Locate and identify every blood parasite.
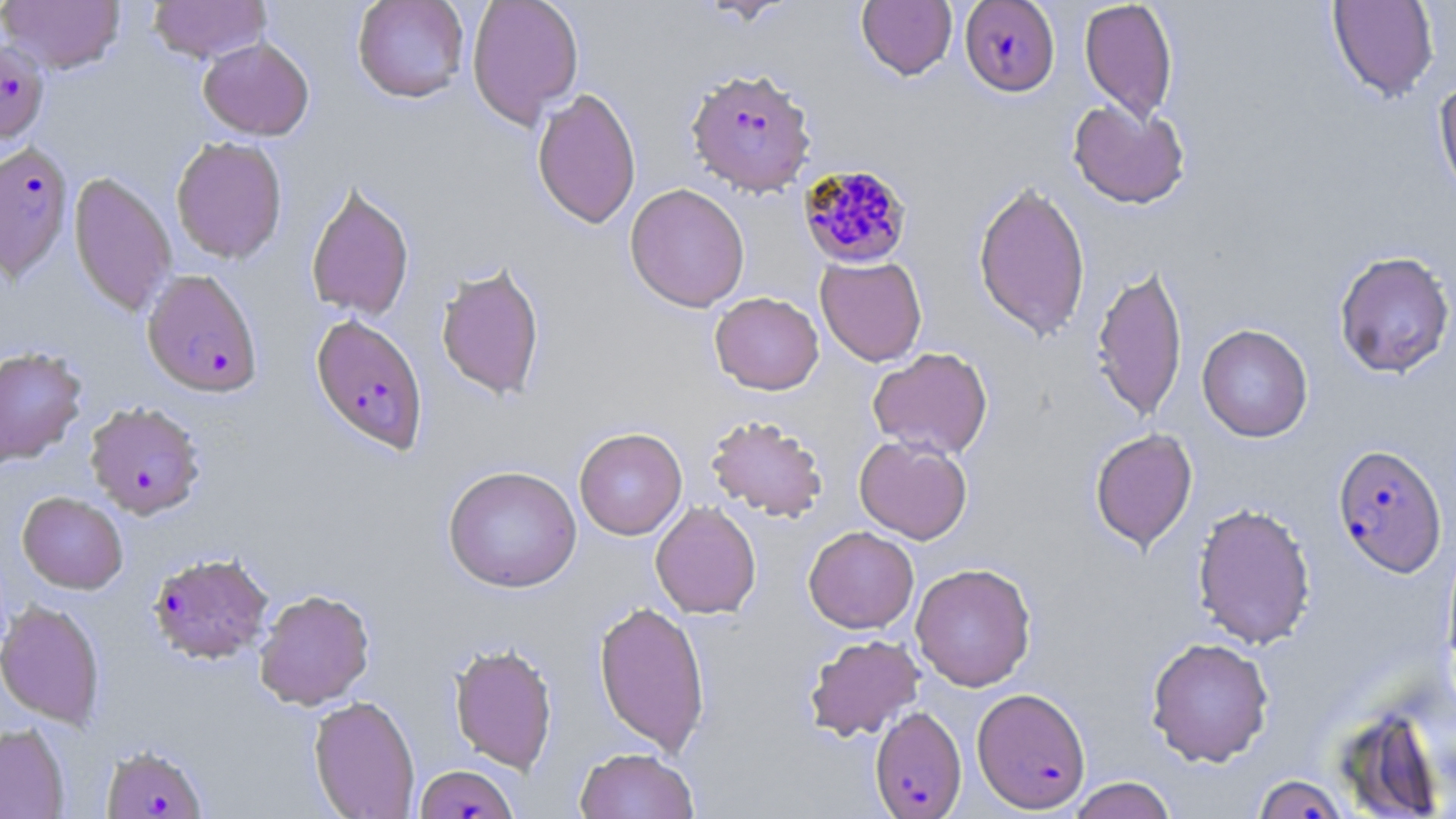

Approximate bounding boxes as (x1,y1)-(x2,y2) corner pairs in pixels.
Plasmodium falciparum-infected red blood cells: (959,0)-(1060,97), (0,38)-(50,144), (685,68)-(817,196), (0,142)-(73,282), (798,164)-(914,269), (142,269)-(263,398), (310,313)-(429,455), (89,400)-(210,517), (1333,444)-(1448,577), (147,551)-(274,665), (972,687)-(1091,812), (870,705)-(967,819), (100,746)-(207,819), (415,764)-(519,819), (1252,773)-(1350,818).
No Plasmodium ovale, Plasmodium malariae, Plasmodium vivax, Babesia divergens, or Trypanosoma brucei observed.

Uninfected red blood cell locations: (1,0)-(125,74), (147,0)-(272,63), (352,0)-(470,103), (466,0)-(584,128), (856,0)-(957,81), (1079,0)-(1178,122), (1327,0)-(1439,103), (198,37)-(314,140), (1433,78)-(1456,201), (532,86)-(641,230), (1068,100)-(1190,209), (170,136)-(288,264), (68,170)-(177,317), (972,179)-(1091,341), (304,182)-(415,321), (624,183)-(750,312), (1333,250)-(1455,378), (816,256)-(927,366), (1090,262)-(1188,423), (435,263)-(545,400), (710,292)-(824,395), (1196,324)-(1314,442), (0,346)-(87,466), (867,346)-(993,460), (705,414)-(829,522), (574,427)-(687,540), (1089,428)-(1197,553), (854,435)-(972,544), (443,465)-(582,593), (17,491)-(128,594), (650,501)-(761,619), (1192,501)-(1316,650), (803,526)-(919,634), (911,562)-(1036,691), (254,589)-(375,709), (0,600)-(106,728), (593,600)-(711,756), (803,633)-(925,741), (1145,636)-(1274,766), (449,641)-(558,773), (308,695)-(420,819), (0,723)-(69,818), (574,746)-(700,819), (1067,777)-(1177,819). Slide-level diagnosis: Plasmodium falciparum. Single field of view. May-Grünwald-Giemsa-stained preparation. Thin blood film. Captured at 1000x magnification. Light microscopy. Image is 1456×819 pixels.